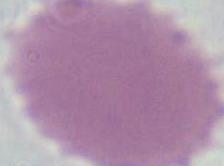 An erythrocyte is shown. Captured at 1000x magnification. Photomicrograph.